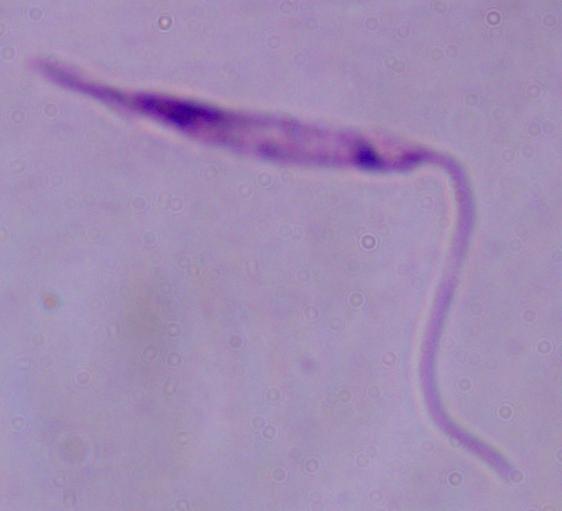

Photomicrograph. 1000x magnification. A Leishmania parasite is seen.